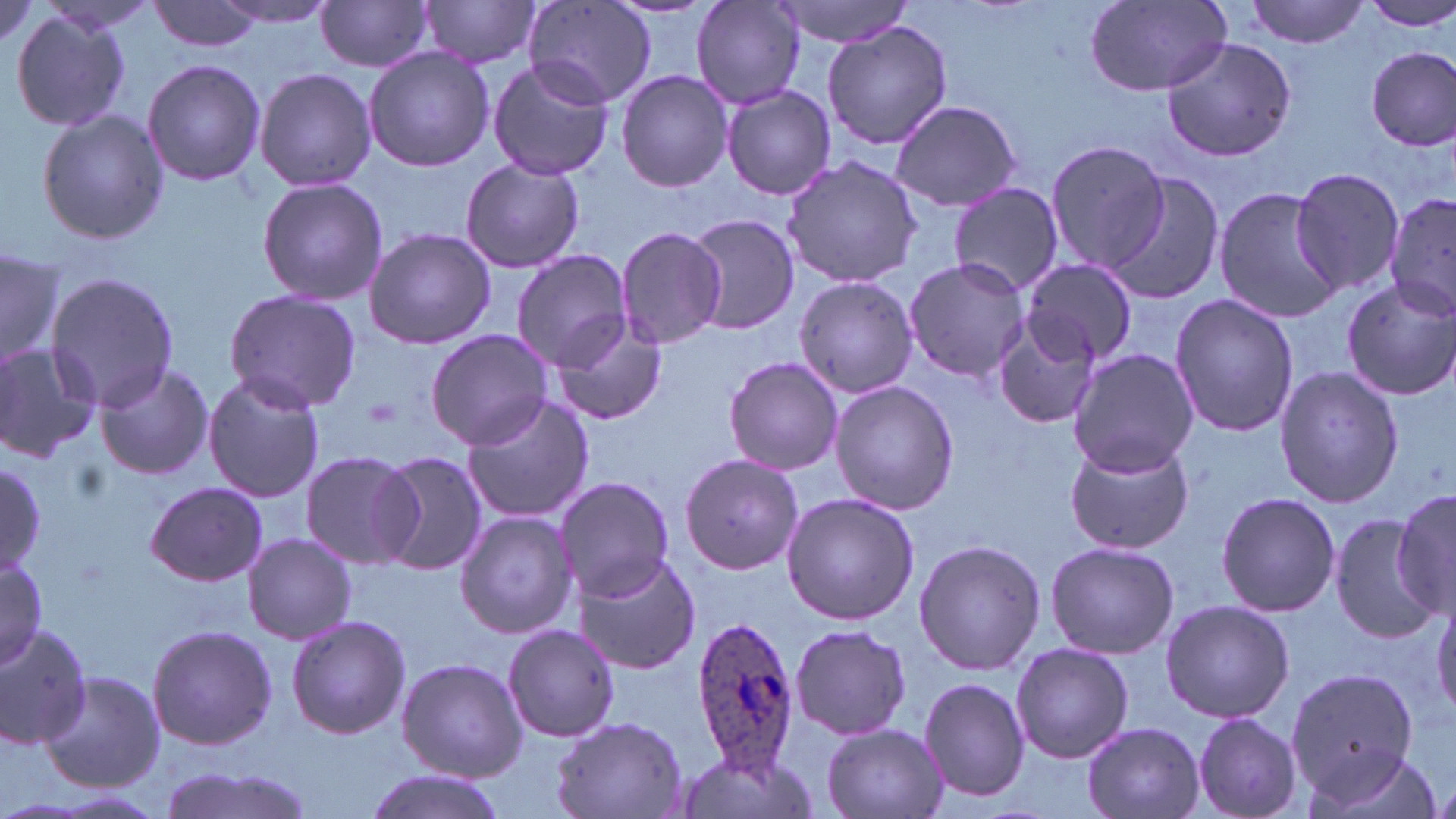

Summary:
  - Coordinate format: approximate bounding boxes as [x1, y1, x2, y2] in pixels
  - Uninfected red blood cell locations: [423, 0, 543, 71], [771, 0, 923, 48], [1244, 0, 1369, 48], [1361, 0, 1456, 30], [148, 1, 263, 54], [315, 1, 436, 73], [524, 1, 656, 107], [693, 1, 806, 110], [1083, 1, 1232, 96], [214, 3, 340, 29], [10, 11, 132, 133], [821, 19, 953, 151], [1162, 36, 1297, 164], [363, 46, 494, 172], [1368, 46, 1455, 152], [486, 58, 615, 182], [142, 59, 266, 187], [255, 67, 376, 192], [615, 69, 734, 193], [722, 85, 836, 200], [890, 99, 1025, 212], [35, 107, 168, 244], [1046, 140, 1171, 274], [781, 155, 924, 287], [460, 158, 584, 274], [1286, 165, 1406, 295], [1107, 172, 1226, 306], [255, 175, 388, 306], [949, 182, 1064, 298], [1213, 186, 1347, 323], [1384, 190, 1456, 323], [687, 215, 802, 335], [615, 225, 728, 352], [363, 227, 496, 349], [0, 246, 64, 368], [511, 249, 633, 370], [903, 257, 1029, 383], [1020, 259, 1137, 366], [44, 272, 182, 410], [794, 277, 917, 398], [1342, 279, 1456, 400], [223, 290, 363, 412], [1168, 293, 1298, 438], [548, 316, 668, 426], [993, 317, 1102, 430], [425, 330, 554, 449], [0, 343, 103, 461], [1067, 348, 1200, 476], [723, 356, 844, 475], [94, 361, 214, 481], [1273, 366, 1403, 507], [202, 373, 327, 503], [830, 381, 957, 516], [461, 391, 593, 524], [1064, 437, 1194, 555], [298, 450, 420, 569], [371, 451, 487, 574], [680, 451, 806, 573], [0, 463, 47, 572], [554, 476, 676, 600], [145, 481, 268, 586], [1393, 486, 1456, 616], [1216, 491, 1342, 618], [780, 492, 919, 625], [454, 510, 579, 641], [1330, 515, 1441, 643], [243, 532, 357, 644], [914, 538, 1045, 674], [1045, 540, 1178, 659], [569, 551, 701, 675], [0, 555, 47, 667], [1431, 596, 1456, 721], [1159, 598, 1294, 723], [285, 614, 410, 741], [0, 623, 96, 749], [146, 623, 278, 752], [502, 624, 620, 743], [789, 624, 911, 741], [1010, 642, 1133, 763], [395, 657, 526, 782], [1286, 667, 1419, 795], [40, 671, 165, 793], [919, 676, 1030, 804], [1191, 712, 1303, 818], [552, 716, 688, 818], [1082, 721, 1206, 819], [820, 722, 948, 819], [1307, 749, 1444, 819], [675, 750, 810, 819], [155, 766, 320, 819], [360, 771, 506, 819]
  - Plasmodium ovale-infected red blood cell locations: [689, 617, 801, 775]
  - Slide-level diagnosis: Plasmodium ovale
  - Field of view: one of a larger specimen
  - Image size: 1456×819 pixels
  - Preparation: thin blood film
  - Magnification: 1000x
  - Modality: optical microscopy
  - Stain: May-Grünwald-Giemsa